Assess the morphology of the red blood cells.
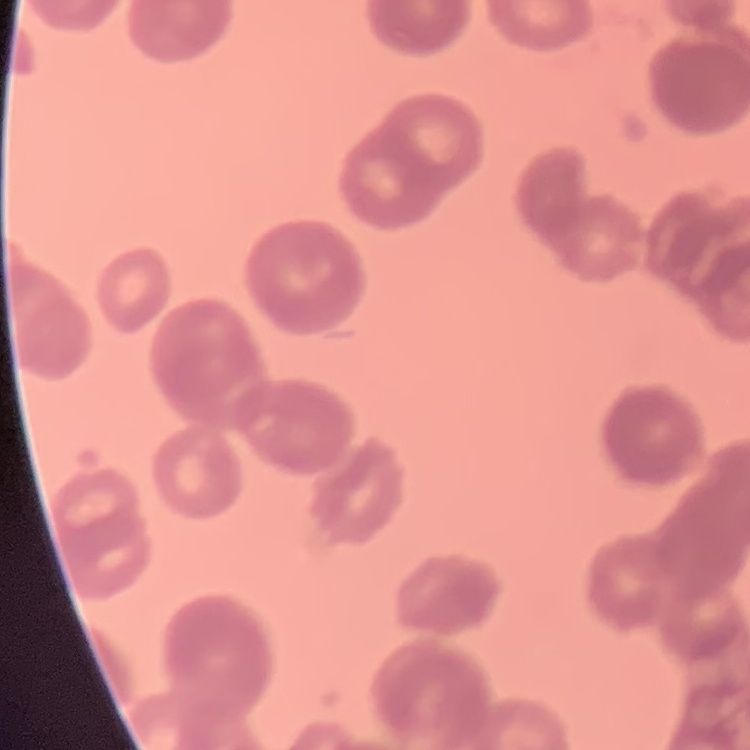
Rouleaux formation.

Thin blood film. Stained with either Field's or Giemsa. Square crop of a larger photomicrograph.